Report the malaria status of this cell.
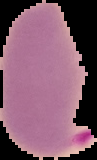
Parasitized.

{
  "image_size": "97×160 pixels",
  "preparation": "thin blood smear",
  "image_type": "segmented cell region with the area outside set to black"
}